Name the parasite shown.
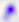

This is Toxoplasma gondii.

Micrograph. Captured at 400x magnification.